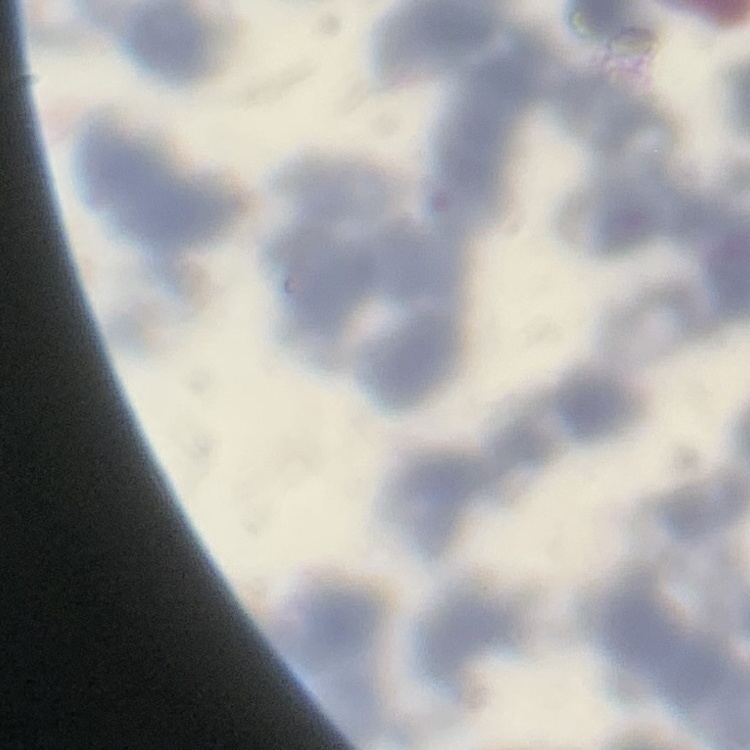

Summary:
  - Red blood cell morphology: rouleaux formation
  - Preparation: thin blood smear
  - Image type: square crop of a larger photomicrograph
  - Stain: Field's or Giemsa